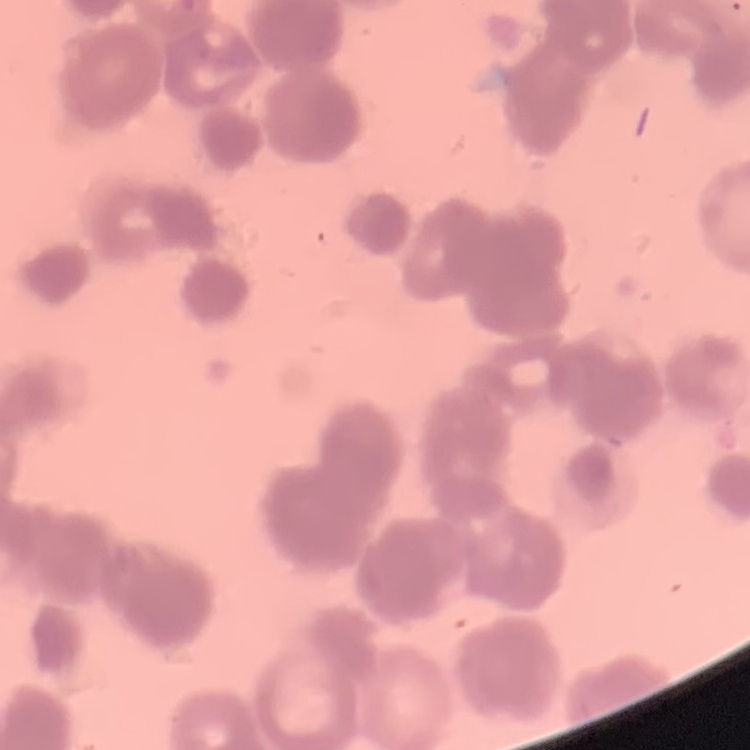

Summary:
  - Red blood cell morphology: rouleaux formation
  - Preparation: thin blood smear
  - Stain: Field's or Giemsa
  - Image type: square crop of a larger photomicrograph